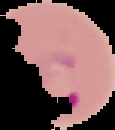

Summary:
  - Result: malaria parasites identified
  - Image type: cell region segmented out of the field of view; surrounding area masked to black
  - Image size: 115×130 pixels
  - Preparation: thin blood smear